Locate and identify every blood parasite.
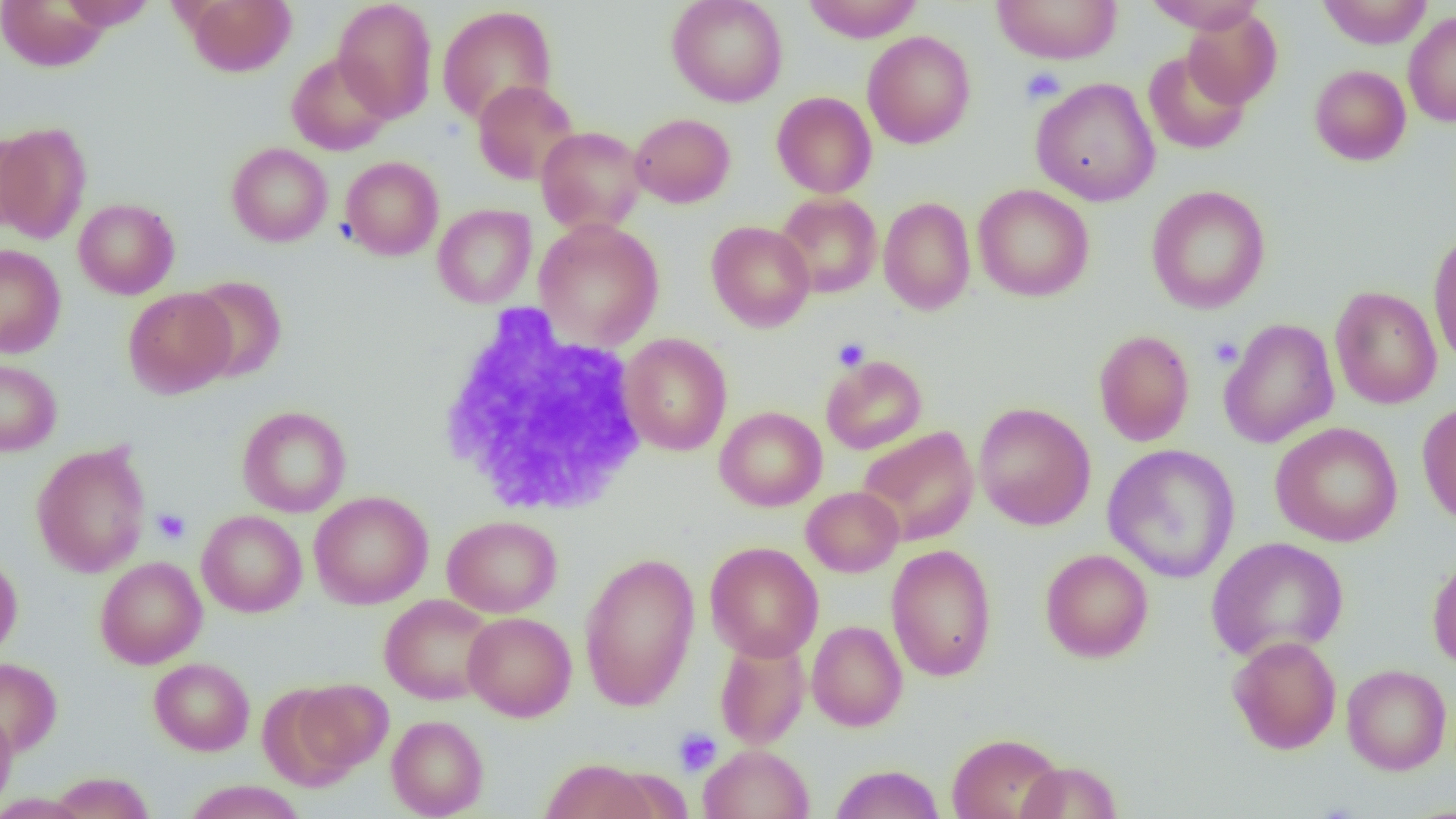

No blood parasites observed.

Approximate bounding boxes as (x1,y1)-(x2,y2) corner pairs in pixels. Platelet locations: (1020,67)-(1066,105), (1209,336)-(1243,368), (832,337)-(870,371), (152,508)-(191,545), (673,728)-(722,777). White blood cell locations: (436,307)-(651,518). Uninfected red blood cell locations: (1,0)-(111,72), (58,0)-(158,30), (183,0)-(296,77), (332,0)-(438,122), (666,0)-(788,107), (801,0)-(924,43), (991,0)-(1122,64), (1142,0)-(1267,32), (1318,0)-(1433,48), (436,5)-(558,126), (1182,8)-(1282,107), (1403,11)-(1456,128), (862,31)-(976,150), (1143,50)-(1251,155), (286,52)-(394,155), (1309,64)-(1411,165), (1030,77)-(1160,206), (472,79)-(579,185), (771,91)-(877,198), (630,113)-(736,208), (0,121)-(92,245), (536,126)-(647,234), (0,127)-(36,236), (226,142)-(333,246), (227,153)-(442,251), (340,156)-(444,261), (973,184)-(1095,302), (1146,185)-(1271,314), (775,193)-(882,299), (878,196)-(975,314), (73,198)-(180,299), (433,204)-(536,308), (534,219)-(665,350), (706,220)-(815,332), (1427,229)-(1456,367), (0,244)-(66,358), (185,275)-(287,384), (1330,285)-(1442,409), (123,287)-(236,398), (1219,318)-(1340,449), (1093,329)-(1195,446), (620,333)-(732,456), (820,355)-(927,454), (0,357)-(61,457), (1416,401)-(1456,526), (973,402)-(1096,530), (237,406)-(351,518), (715,406)-(827,511), (1270,421)-(1403,547), (856,426)-(979,546), (31,443)-(151,577), (1102,444)-(1240,583), (802,486)-(904,577), (309,491)-(434,609), (197,510)-(307,617), (442,515)-(562,617), (1206,537)-(1349,663), (705,542)-(824,661), (885,544)-(997,682), (1040,548)-(1153,663), (579,552)-(700,712), (0,553)-(23,661), (1427,553)-(1456,671), (95,556)-(207,669), (379,594)-(497,705), (462,612)-(576,721), (807,620)-(907,732), (1227,635)-(1342,754), (714,636)-(810,750), (0,657)-(62,757), (149,658)-(254,755), (1342,664)-(1452,775), (287,678)-(393,779), (0,707)-(17,814), (386,715)-(489,818), (948,732)-(1066,819), (698,744)-(814,819), (541,757)-(657,819), (1016,760)-(1123,819), (831,764)-(944,819), (49,771)-(155,818), (183,780)-(306,819), (0,793)-(90,819). Slide-level diagnosis: no evidence of blood parasites. Light microscopy. One field of a larger specimen. Captured at 1000x magnification. Thin blood smear. Image is 1456×819 pixels.